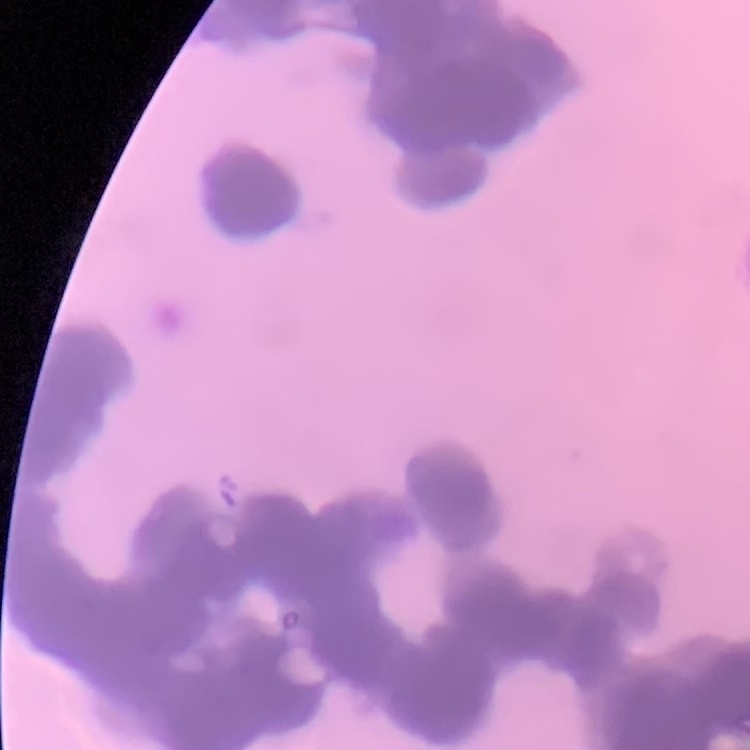
The erythrocytes show rouleaux formation. One tile cut from a larger photomicrograph. Thin blood film. Stained with either Field's or Giemsa.